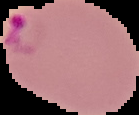

The area outside the segmented cell region is set to black. From a thin blood film. Malaria status: parasitized. Image is 139×115 pixels.